Report the malaria status of this cell.
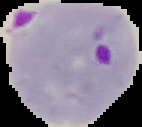
Parasitized.

Summary:
  - Preparation: thin blood smear
  - Image type: segmented cell region on a black background
  - Image size: 142×127 pixels